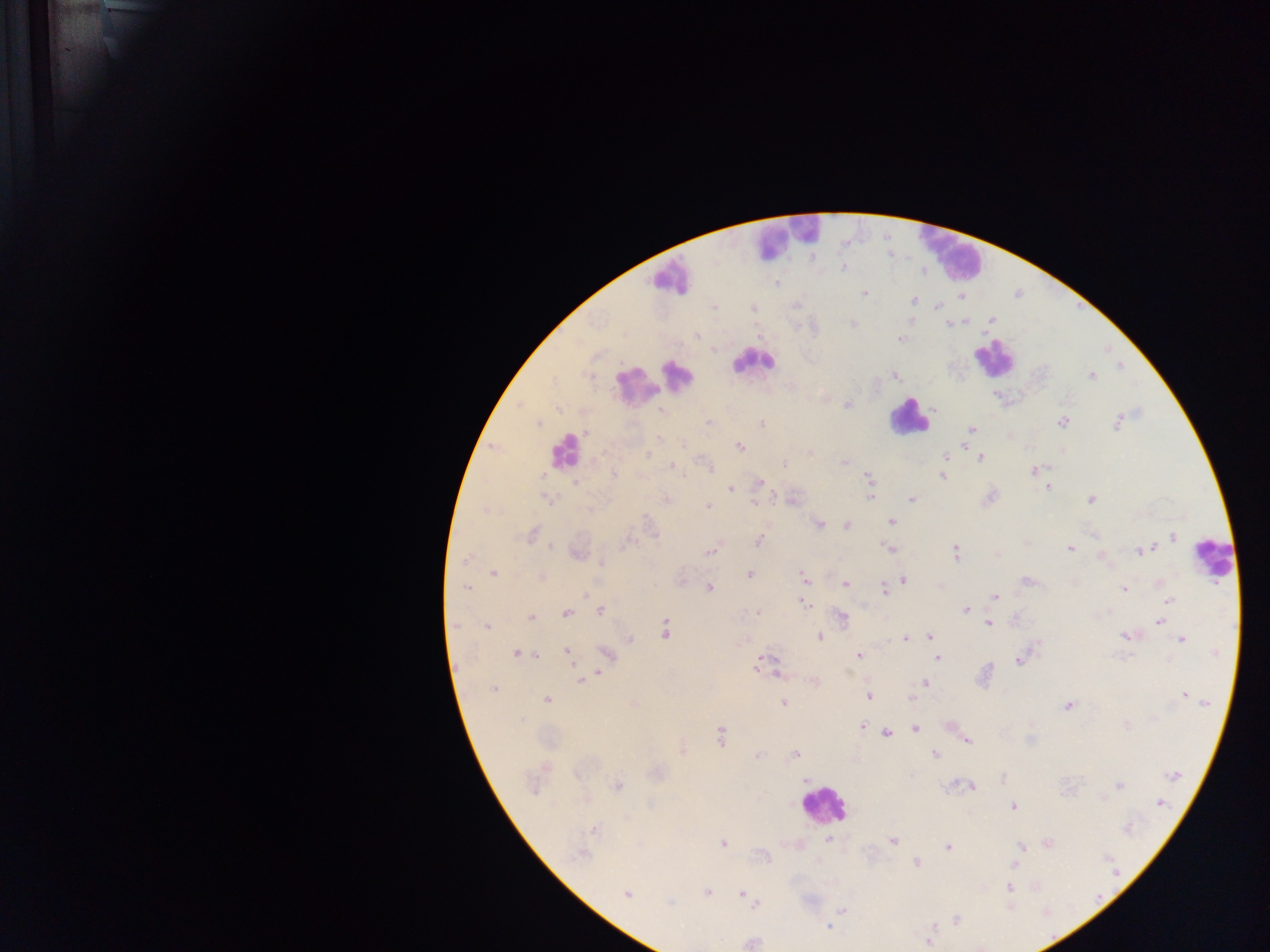
preparation = thick blood smear
country = Ghana
Plasmodium parasite locations = approximate centers as {x, y} in pixels: {843, 268}, {777, 283}, {864, 293}, {962, 297}, {913, 301}, {797, 306}, {937, 306}, {713, 307}, {753, 308}, {992, 320}, {852, 323}, {948, 324}, {697, 335}, {900, 339}, {895, 376}, {1092, 376}, {846, 404}, {935, 410}, {662, 411}, {709, 422}, {1062, 422}, {539, 423}, {762, 423}, {1117, 423}, {971, 429}, {584, 433}, {659, 438}, {683, 445}, {740, 446}, {810, 453}, {603, 454}, {950, 454}, {648, 455}, {946, 457}, {980, 459}, {844, 462}, {785, 464}, {672, 465}, {709, 466}, {1034, 470}, {614, 474}, {942, 476}, {869, 478}, {575, 482}, {759, 483}, {1048, 487}, {731, 489}, {990, 497}, {870, 498}, {667, 499}, {912, 499}, {548, 500}, {1091, 500}, {755, 503}, {707, 507}, {590, 510}, {647, 518}, {892, 521}, {819, 524}, {847, 526}, {532, 534}, {1172, 537}, {759, 541}, {628, 542}, {551, 547}, {889, 548}, {1069, 548}, {1144, 550}, {710, 552}, {955, 552}, {577, 555}, {997, 555}, {1101, 557}, {467, 558}, {602, 563}, {494, 573}, {750, 575}, {541, 577}, {804, 578}, {904, 580}, {1027, 581}, {1160, 583}, {845, 585}, {466, 588}, {709, 588}, {884, 589}, {1124, 589}, {585, 594}, {995, 596}, {1168, 600}, {803, 603}, {601, 610}, {965, 610}, {758, 611}, {566, 613}, {1163, 615}, {532, 618}, {842, 618}, {1159, 621}, {989, 623}, {455, 625}, {487, 627}, {666, 629}, {819, 636}, {1125, 636}, {930, 637}, {905, 638}, {629, 639}, {1182, 640}, {1037, 645}, {566, 651}, {516, 654}, {537, 655}, {606, 655}, {858, 656}, {938, 658}, {1018, 660}, {766, 663}, {759, 666}, {598, 673}, {594, 676}, {582, 680}, {925, 682}, {814, 683}, {493, 690}, {1184, 695}, {869, 697}, {909, 697}, {546, 700}, {1202, 701}, {783, 703}, {1068, 705}, {522, 720}, {1127, 725}, {862, 727}, {916, 729}, {886, 733}, {720, 735}, {967, 741}, {682, 752}, {935, 754}, {757, 755}, {795, 755}, {577, 773}, {1173, 775}, {1003, 778}, {807, 779}, {617, 786}, {971, 786}, {1119, 786}, {1160, 803}, {1014, 807}, {1129, 829}, {594, 830}, {827, 839}, {892, 841}, {723, 843}, {1048, 844}, {1020, 846}, {948, 847}, {582, 855}, {917, 863}, {1014, 864}, {1010, 888}, {707, 892}, {627, 894}, {742, 894}, {669, 903}, {755, 903}, {1010, 906}, {842, 910}, {957, 920}, {827, 927}, {930, 939}, {752, 943}
capture = mobile-phone photograph through a microscope
image size = 1270×952 pixels
leukocyte locations = approximate centers as {x, y} in pixels: {782, 237}, {950, 251}, {669, 276}, {993, 357}, {752, 361}, {678, 374}, {635, 386}, {907, 417}, {564, 451}, {1212, 559}, {824, 805}
field of view = single